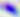
{
  "identification": "Toxoplasma gondii",
  "modality": "micrograph",
  "magnification": "400x"
}